State which cell type is depicted.
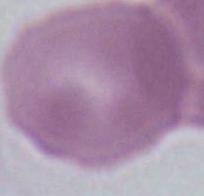

An erythrocyte.

Micrograph. Captured at 1000x magnification.